Describe the morphology of the red blood cells.
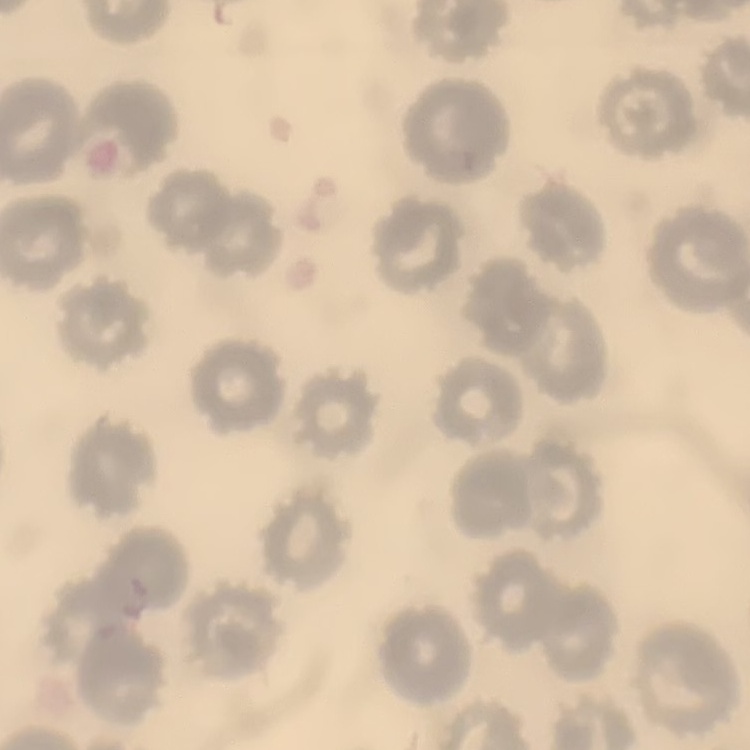
They show no rouleaux formation.

image type = square crop of a larger photomicrograph
stain = Field's or Giemsa
preparation = thin blood smear